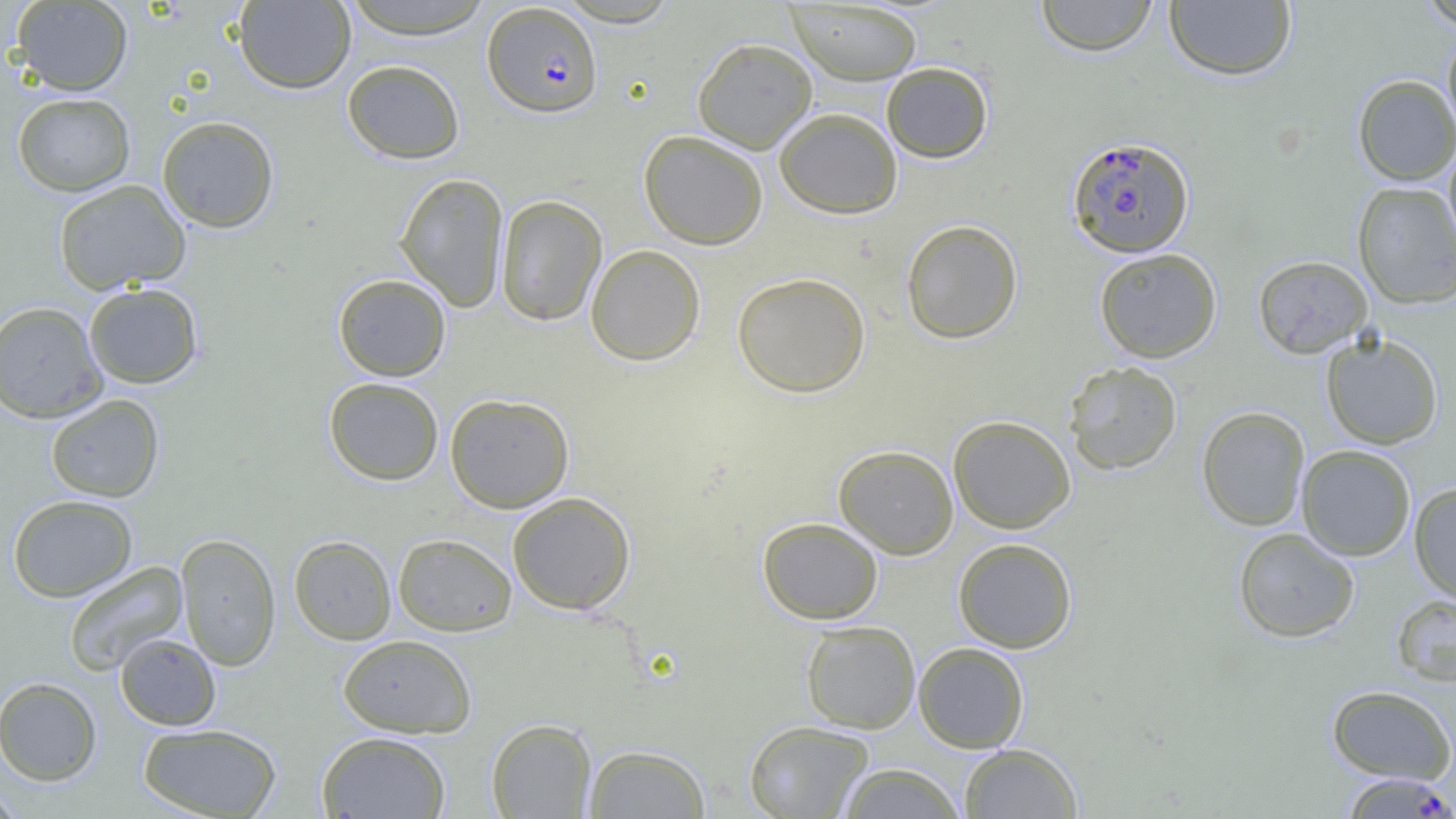
Approximate bounding boxes as [x1, y1, x2, y2] in pixels. Plasmodium falciparum-infected red blood cell locations: [482, 2, 603, 118], [1066, 135, 1194, 258], [1340, 772, 1455, 818]. Uninfected red blood cell locations: [338, 0, 496, 39], [555, 0, 682, 27], [1035, 0, 1159, 56], [1164, 0, 1298, 82], [1417, 0, 1456, 31], [10, 1, 133, 96], [234, 1, 355, 94], [786, 1, 922, 85], [1442, 27, 1456, 139], [692, 37, 817, 154], [342, 59, 465, 164], [881, 61, 994, 164], [1353, 75, 1456, 185], [12, 92, 135, 196], [774, 107, 902, 219], [156, 116, 280, 233], [639, 130, 768, 250], [1442, 140, 1456, 261], [394, 172, 509, 311], [53, 179, 191, 295], [1352, 180, 1456, 309], [495, 195, 607, 327], [901, 219, 1023, 344], [585, 244, 706, 366], [1093, 247, 1223, 363], [1253, 255, 1372, 358], [732, 272, 871, 398], [333, 273, 451, 381], [83, 283, 204, 389], [0, 300, 108, 423], [1311, 333, 1426, 561], [1320, 333, 1444, 450], [1063, 360, 1183, 476], [323, 377, 444, 486], [444, 393, 575, 513], [46, 394, 165, 502], [1196, 406, 1310, 531], [947, 415, 1076, 534], [833, 444, 959, 559], [1296, 445, 1416, 561], [1408, 482, 1456, 604], [507, 491, 636, 615], [7, 494, 138, 602], [757, 517, 884, 624], [1232, 527, 1360, 643], [175, 533, 281, 671], [392, 533, 517, 636], [288, 535, 397, 645], [952, 537, 1078, 653], [63, 561, 189, 676], [1391, 594, 1456, 687], [800, 620, 921, 734], [115, 633, 222, 731], [337, 634, 478, 738], [913, 642, 1029, 753], [0, 676, 102, 786], [1327, 684, 1455, 784], [485, 717, 597, 818], [743, 720, 874, 818], [137, 723, 283, 818], [316, 731, 451, 818], [958, 742, 1082, 818], [582, 744, 711, 818], [837, 763, 965, 819], [0, 783, 25, 819]. Slide-level diagnosis: Plasmodium falciparum. One field of a larger specimen. Thin blood smear. Optical microscopy. Captured at 1000x magnification. Image is 1456×819 pixels.